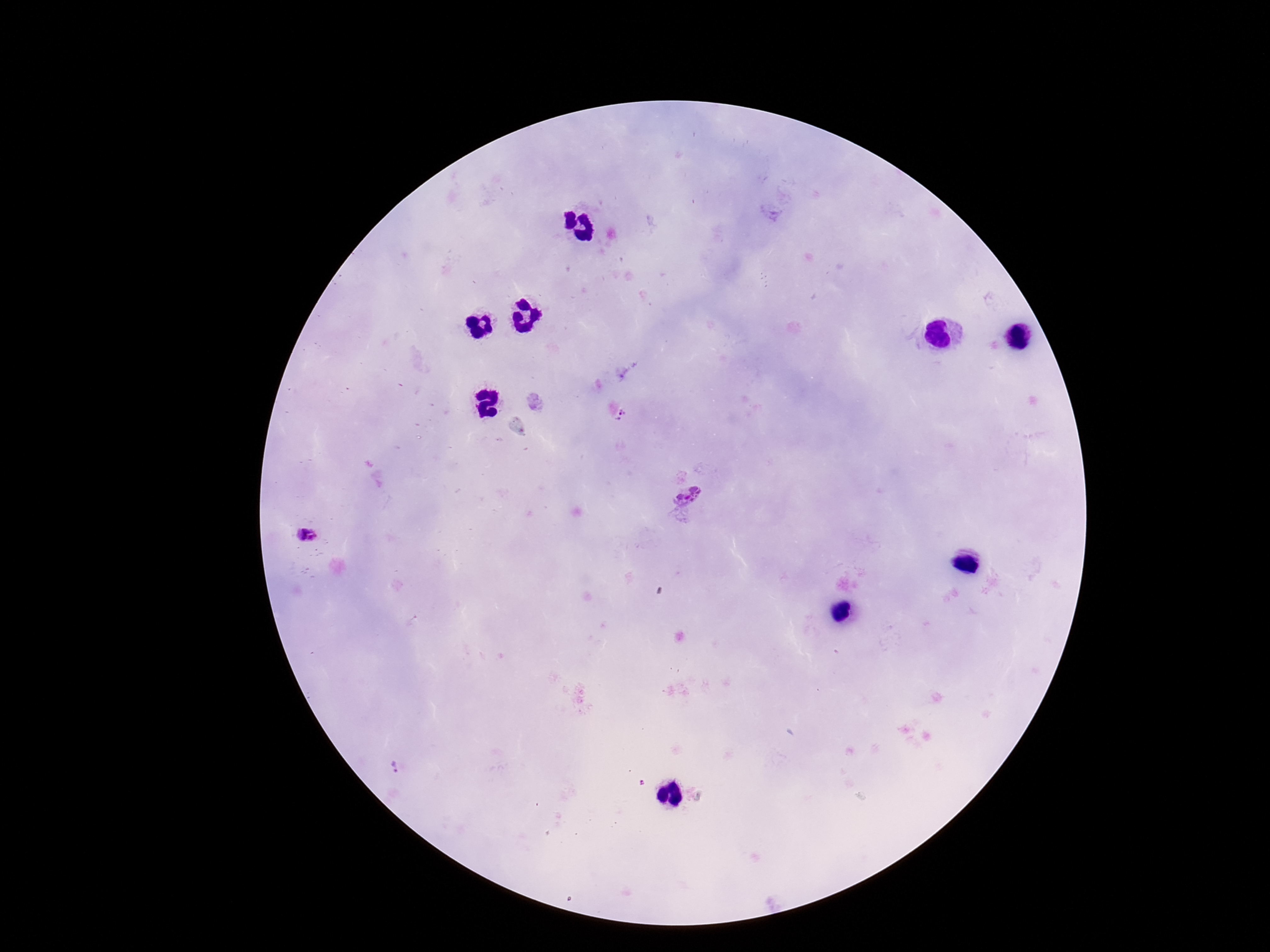

Approximate centers as {x, y} in pixels. Plasmodium parasite locations: {622, 415}, {688, 494}, {310, 536}, {397, 767}. Patient malaria status: infected. Image is 1270×952 pixels. Giemsa-stained preparation. Photographed through the microscope eyepiece with a smartphone camera. 100x magnification. One field from this slide. Thick blood film.